Mark where platelets are.
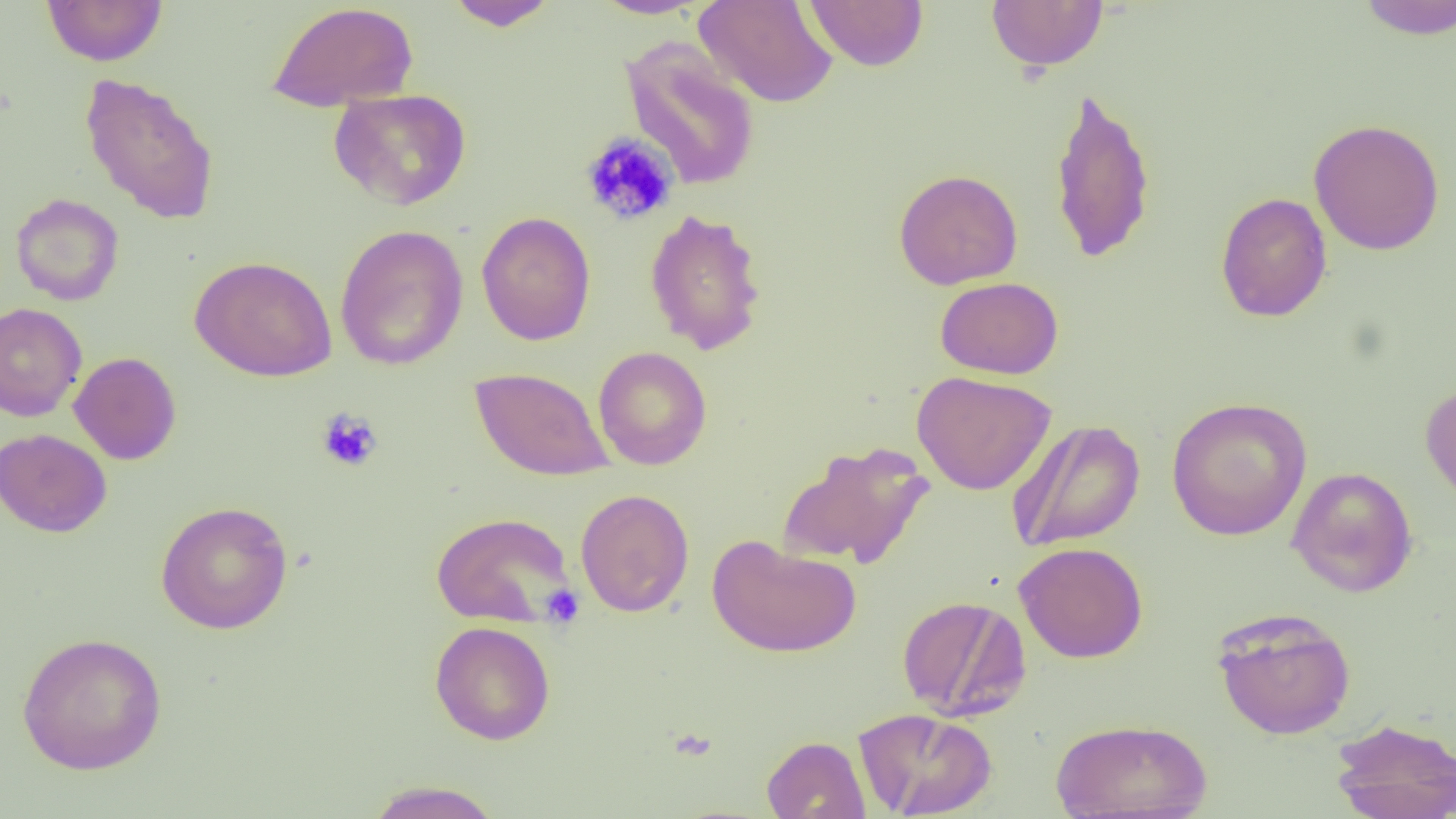

Approximate bounding boxes as (x1, y1, x2, y2) in pixels.
Platelets: (579, 131, 679, 226), (316, 409, 382, 472), (540, 585, 585, 627).

Summary:
  - Uninfected red blood cell locations: (42, 0, 167, 66), (444, 0, 560, 30), (590, 0, 712, 19), (695, 0, 839, 108), (804, 0, 928, 71), (1354, 0, 1456, 39), (266, 1, 420, 112), (986, 1, 1109, 72), (620, 37, 761, 191), (79, 72, 220, 225), (1048, 84, 1158, 266), (328, 88, 472, 210), (1308, 118, 1445, 256), (893, 168, 1023, 289), (1215, 192, 1332, 322), (10, 193, 124, 306), (644, 208, 767, 356), (476, 211, 596, 346), (335, 223, 469, 371), (189, 255, 338, 382), (935, 277, 1063, 380), (0, 302, 87, 422), (593, 347, 713, 470), (69, 352, 181, 465), (470, 366, 614, 482), (912, 371, 1056, 495), (1420, 381, 1456, 512), (1166, 396, 1312, 541), (1006, 419, 1146, 552), (0, 428, 112, 538), (778, 441, 936, 570), (1287, 466, 1418, 597), (575, 489, 694, 617), (155, 500, 293, 634), (431, 511, 577, 628), (707, 535, 861, 658), (1014, 541, 1149, 663), (895, 594, 1031, 721), (1211, 607, 1357, 741), (429, 621, 556, 745), (16, 631, 167, 774), (854, 707, 997, 819), (1050, 717, 1212, 818), (1330, 717, 1456, 819), (761, 735, 870, 819), (364, 780, 504, 818)
  - Slide-level diagnosis: negative for blood parasites
  - Field of view: single
  - Preparation: thin blood smear
  - Modality: optical microscopy
  - Magnification: 1000x
  - Image size: 1456×819 pixels